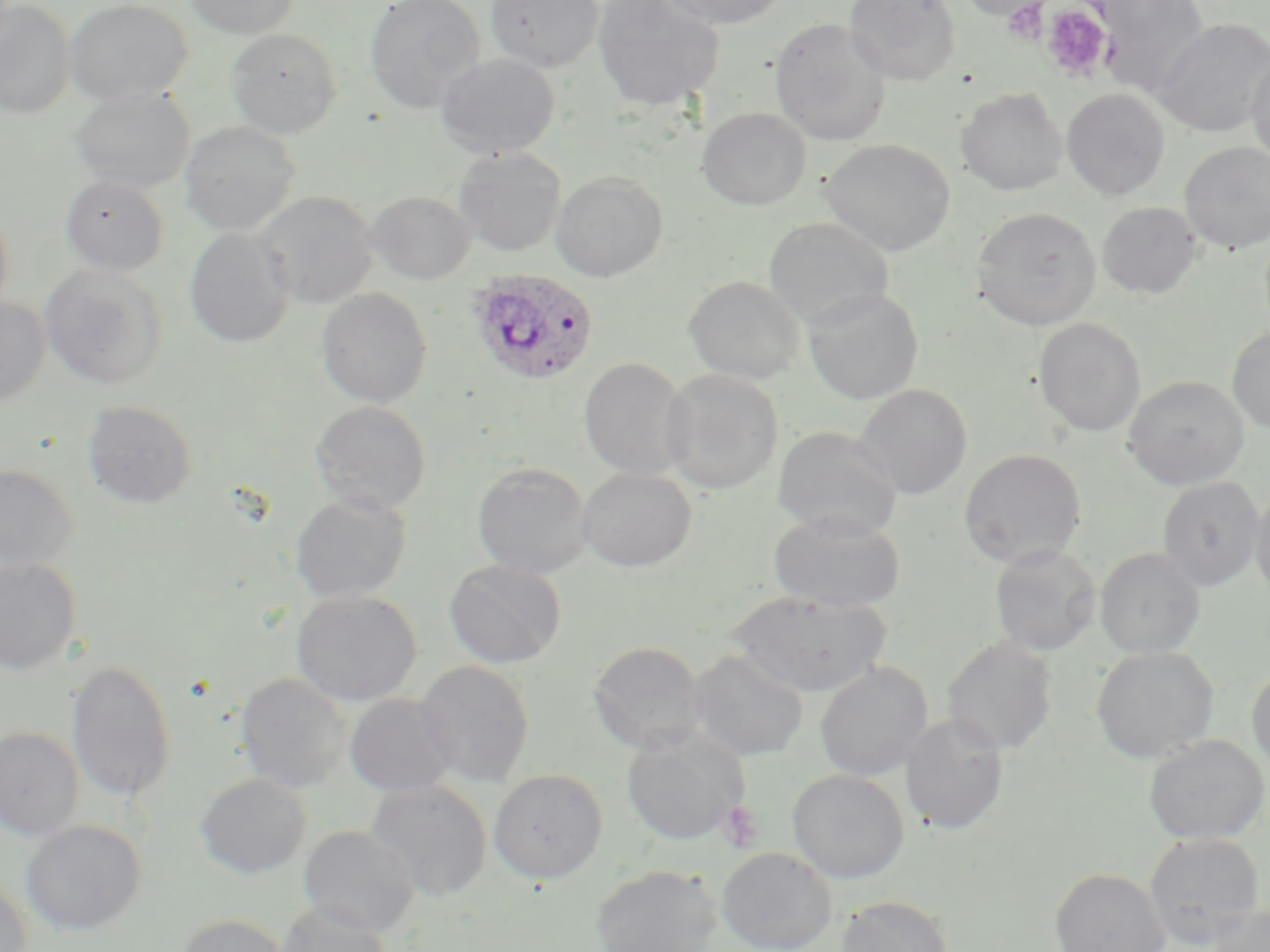

Approximate bounding boxes as named x1/y1/x2/y2 corners in pixels. Platelet locations: (x1=1004, y1=2, x2=1052, y2=43), (x1=1040, y1=4, x2=1114, y2=83), (x1=718, y1=800, x2=763, y2=852). Uninfected red blood cell locations: (x1=0, y1=0, x2=75, y2=119), (x1=65, y1=0, x2=193, y2=106), (x1=184, y1=0, x2=299, y2=38), (x1=364, y1=0, x2=486, y2=115), (x1=484, y1=0, x2=604, y2=73), (x1=592, y1=0, x2=725, y2=111), (x1=657, y1=0, x2=791, y2=29), (x1=844, y1=0, x2=961, y2=85), (x1=955, y1=0, x2=1050, y2=20), (x1=1096, y1=0, x2=1209, y2=96), (x1=1000, y1=2, x2=1055, y2=38), (x1=769, y1=17, x2=892, y2=146), (x1=1153, y1=18, x2=1270, y2=137), (x1=225, y1=28, x2=342, y2=138), (x1=1246, y1=48, x2=1270, y2=167), (x1=435, y1=54, x2=560, y2=158), (x1=69, y1=87, x2=195, y2=193), (x1=955, y1=87, x2=1067, y2=195), (x1=1061, y1=88, x2=1170, y2=200), (x1=697, y1=107, x2=811, y2=210), (x1=179, y1=121, x2=299, y2=237), (x1=820, y1=138, x2=955, y2=256), (x1=1179, y1=142, x2=1270, y2=253), (x1=453, y1=148, x2=566, y2=257), (x1=550, y1=170, x2=669, y2=282), (x1=60, y1=175, x2=169, y2=275), (x1=255, y1=191, x2=379, y2=308), (x1=366, y1=191, x2=477, y2=283), (x1=1097, y1=201, x2=1202, y2=299), (x1=0, y1=205, x2=14, y2=316), (x1=971, y1=207, x2=1102, y2=330), (x1=764, y1=216, x2=894, y2=328), (x1=184, y1=227, x2=295, y2=348), (x1=40, y1=264, x2=168, y2=390), (x1=683, y1=276, x2=805, y2=384), (x1=317, y1=287, x2=432, y2=408), (x1=803, y1=288, x2=924, y2=406), (x1=0, y1=298, x2=50, y2=407), (x1=1034, y1=318, x2=1146, y2=437), (x1=1227, y1=326, x2=1270, y2=433), (x1=578, y1=357, x2=692, y2=480), (x1=661, y1=368, x2=783, y2=494), (x1=1124, y1=375, x2=1249, y2=490), (x1=856, y1=383, x2=973, y2=500), (x1=310, y1=400, x2=432, y2=516), (x1=82, y1=401, x2=197, y2=508), (x1=772, y1=425, x2=902, y2=539), (x1=959, y1=449, x2=1087, y2=568), (x1=472, y1=462, x2=592, y2=579), (x1=0, y1=464, x2=79, y2=573), (x1=577, y1=467, x2=697, y2=572), (x1=1157, y1=477, x2=1264, y2=591), (x1=1251, y1=485, x2=1270, y2=606), (x1=290, y1=493, x2=411, y2=604), (x1=768, y1=511, x2=905, y2=613), (x1=989, y1=544, x2=1101, y2=656), (x1=1095, y1=547, x2=1205, y2=658), (x1=0, y1=556, x2=83, y2=676), (x1=444, y1=559, x2=566, y2=669), (x1=291, y1=590, x2=421, y2=707), (x1=728, y1=591, x2=891, y2=698), (x1=942, y1=636, x2=1057, y2=756), (x1=587, y1=640, x2=707, y2=754), (x1=1091, y1=646, x2=1218, y2=763), (x1=688, y1=649, x2=809, y2=761), (x1=415, y1=659, x2=535, y2=788), (x1=66, y1=660, x2=176, y2=804), (x1=814, y1=662, x2=933, y2=781), (x1=1247, y1=663, x2=1270, y2=776), (x1=236, y1=672, x2=351, y2=793), (x1=344, y1=693, x2=459, y2=798), (x1=900, y1=714, x2=1009, y2=835), (x1=0, y1=726, x2=84, y2=841), (x1=621, y1=732, x2=748, y2=846), (x1=1144, y1=734, x2=1269, y2=845), (x1=488, y1=768, x2=608, y2=883), (x1=788, y1=769, x2=909, y2=883), (x1=195, y1=773, x2=311, y2=878), (x1=366, y1=780, x2=492, y2=901), (x1=21, y1=819, x2=146, y2=935), (x1=299, y1=826, x2=419, y2=936), (x1=1143, y1=832, x2=1265, y2=948), (x1=717, y1=846, x2=837, y2=952), (x1=590, y1=864, x2=724, y2=952), (x1=1049, y1=867, x2=1170, y2=952), (x1=0, y1=878, x2=32, y2=951), (x1=837, y1=896, x2=954, y2=952), (x1=276, y1=901, x2=391, y2=952), (x1=1204, y1=902, x2=1270, y2=952), (x1=175, y1=914, x2=291, y2=952). Plasmodium ovale-infected red blood cell locations: (x1=467, y1=270, x2=599, y2=386). Slide-level diagnosis: Plasmodium ovale. May-Grünwald-Giemsa stain. Thin blood film. 1000x magnification. Optical microscopy. Image is 1270×952 pixels. One field of a larger specimen.